Give the position of every Plasmodium parasite.
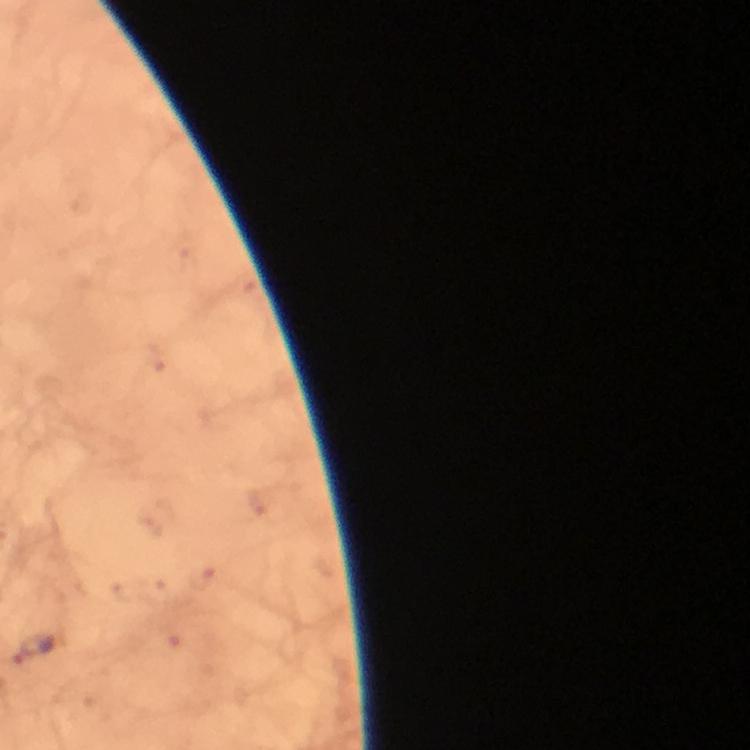

Approximate centers as {x, y} in pixels.
Plasmodium parasites: {30, 651}.

Summary:
  - Preparation: thick smear
  - Immersion oil: applied
  - Stain: Giemsa
  - Image size: 750×750 pixels
  - Context: from a diagnostic examination for malaria
  - Cropped from: one field of view
  - Magnification: 100x
  - Capture: smartphone photograph through a microscope